Give the position of every Plasmodium parasite visible.
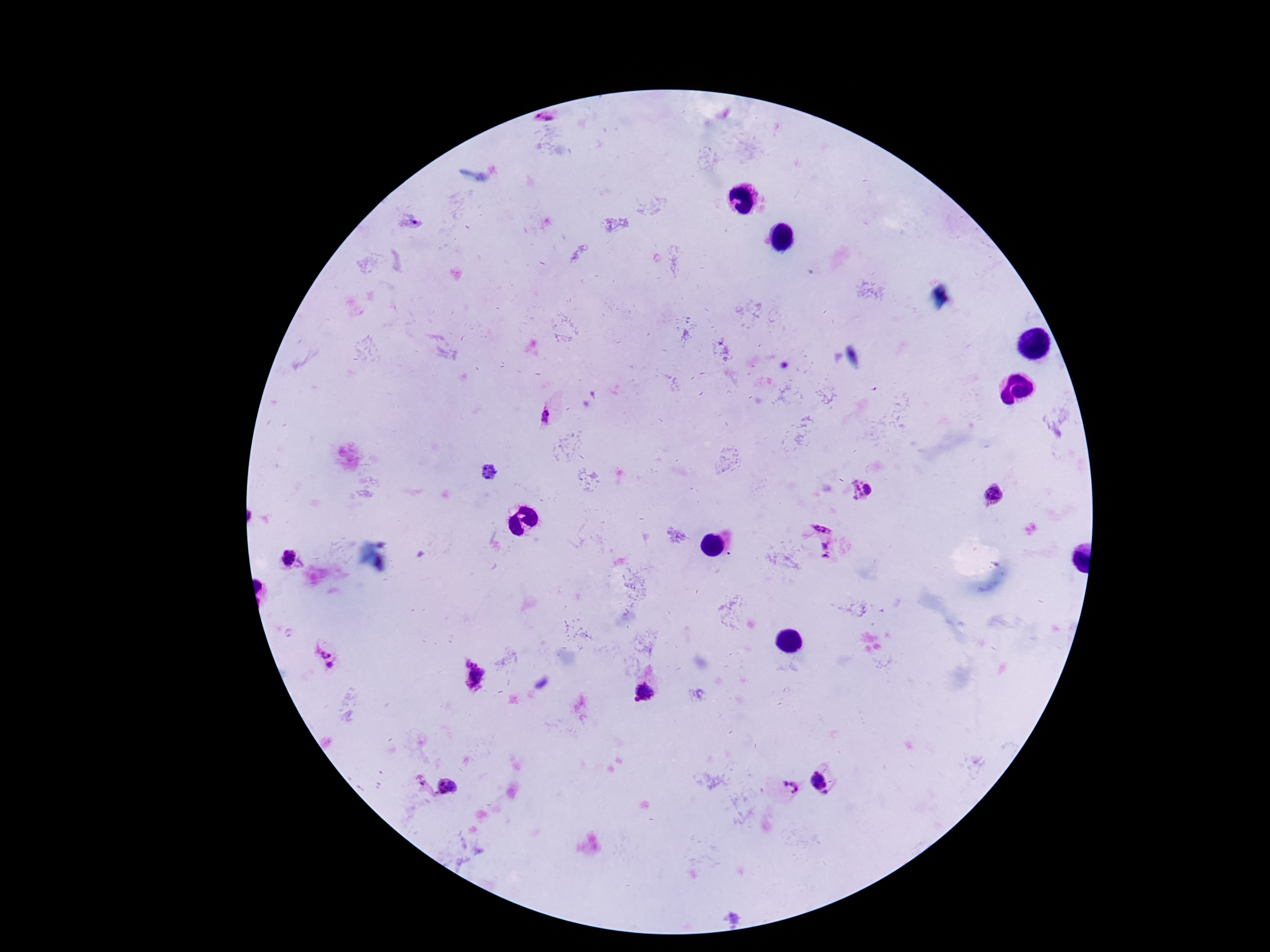
Approximate object centers, in pixels from the top-left corner.
Plasmodium parasites: (x=545, y=120), (x=410, y=223), (x=549, y=415), (x=491, y=473), (x=857, y=489), (x=867, y=489), (x=992, y=493), (x=822, y=524), (x=828, y=550), (x=287, y=558), (x=323, y=652), (x=466, y=661), (x=331, y=667), (x=478, y=676), (x=645, y=692), (x=420, y=779), (x=821, y=783), (x=447, y=786), (x=791, y=789).

{
  "capture": "smartphone camera through the microscope eyepiece",
  "patient_malaria_status": "infected",
  "preparation": "thick blood film",
  "magnification": "100x",
  "field_of_view": "one from this slide",
  "stain": "Giemsa",
  "image_size": "1270×952 pixels"
}